Report the malaria status of this cell.
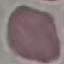

It is uninfected.

Summary:
  - Stain: Giemsa
  - Image type: automatically extracted cell patch, resized to 64 × 64 pixels
  - Preparation: thin blood film
  - Capture: smartphone camera at the microscope eyepiece